Report the malaria status of this cell.
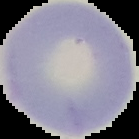

Uninfected.

Image is 139×139 pixels. From a thin blood film. Cell region segmented out of the field of view; the surrounding area is masked to black.